Name the parasite shown.
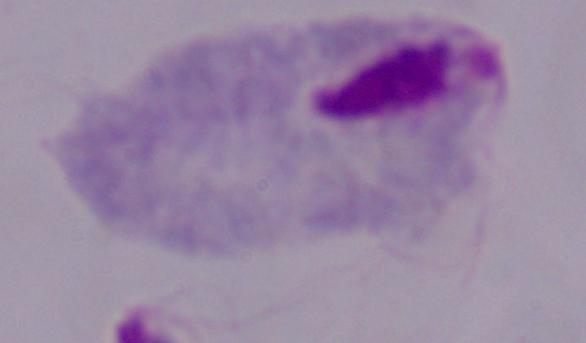

This is a trichomonad.

Captured at 1000x magnification. Photomicrograph.